State the blood parasite species.
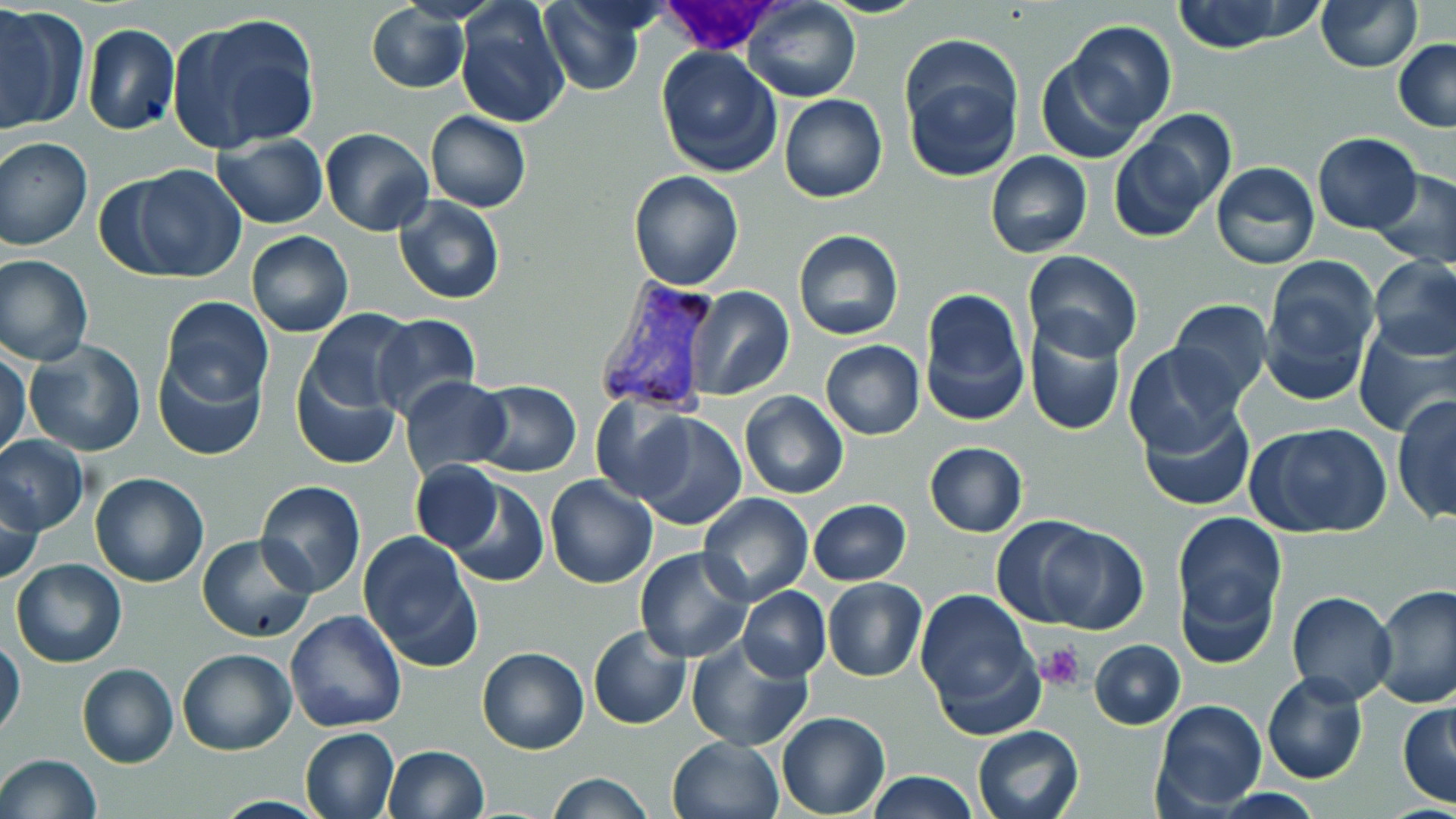

Plasmodium vivax.

Summary:
  - Coordinate format: approximate bounding boxes as [x1, y1, x2, y2] in pixels
  - Platelet locations: [1036, 643, 1085, 691]
  - Plasmodium vivax-infected red blood cell locations: [593, 275, 721, 415]
  - White blood cell locations: [650, 0, 794, 57]
  - Uninfected red blood cell locations: [538, 0, 651, 96], [745, 0, 859, 102], [1316, 0, 1421, 72], [455, 1, 572, 129], [1170, 1, 1319, 54], [0, 4, 87, 133], [367, 4, 471, 93], [169, 13, 322, 153], [1065, 21, 1178, 132], [82, 24, 179, 135], [1393, 39, 1456, 131], [899, 44, 1022, 182], [655, 45, 783, 177], [1034, 54, 1146, 165], [779, 94, 887, 202], [425, 109, 531, 212], [321, 127, 433, 237], [1109, 127, 1224, 240], [213, 133, 329, 229], [1312, 133, 1423, 234], [0, 136, 93, 251], [141, 148, 321, 254], [985, 150, 1092, 258], [1210, 162, 1320, 269], [123, 164, 247, 282], [1372, 169, 1456, 266], [627, 170, 745, 292], [393, 196, 506, 306], [793, 230, 903, 340], [246, 231, 352, 337], [1023, 250, 1143, 360], [1, 254, 94, 367], [1368, 255, 1456, 361], [1259, 257, 1379, 404], [684, 286, 794, 399], [917, 288, 1029, 427], [159, 296, 274, 404], [1167, 299, 1273, 403], [302, 308, 420, 418], [370, 312, 483, 420], [1023, 320, 1128, 438], [1354, 325, 1454, 436], [1025, 328, 1242, 441], [25, 339, 145, 457], [820, 339, 924, 440], [1124, 343, 1246, 456], [0, 346, 29, 461], [154, 352, 266, 461], [290, 358, 403, 470], [401, 375, 511, 481], [471, 379, 582, 476], [740, 391, 848, 499], [1392, 393, 1456, 525], [591, 398, 702, 502], [1139, 403, 1255, 512], [629, 412, 747, 532], [1245, 421, 1394, 539], [0, 435, 87, 535], [923, 441, 1028, 536], [411, 461, 503, 553], [434, 471, 552, 588], [89, 472, 211, 587], [545, 476, 659, 589], [1, 480, 45, 586], [255, 480, 366, 597], [697, 492, 813, 607], [808, 500, 911, 585], [1173, 511, 1286, 642], [991, 515, 1104, 626], [1034, 526, 1150, 634], [358, 531, 484, 674], [195, 532, 317, 644], [633, 548, 754, 663], [10, 558, 127, 668], [1177, 568, 1281, 671], [822, 578, 927, 682], [1371, 581, 1456, 707], [737, 586, 830, 681], [915, 587, 1039, 727], [1285, 591, 1398, 705], [284, 610, 409, 733], [588, 625, 690, 731], [686, 635, 814, 752], [0, 636, 26, 739], [1090, 639, 1186, 729], [476, 646, 589, 755], [177, 648, 296, 755], [77, 663, 178, 767], [1261, 671, 1369, 785], [1153, 700, 1267, 814], [1397, 700, 1456, 808], [776, 711, 889, 817], [972, 723, 1085, 819], [300, 728, 400, 818], [667, 735, 784, 819], [382, 745, 489, 819], [0, 753, 101, 819], [866, 771, 980, 818], [546, 773, 653, 818]
  - Field of view: one of a larger specimen
  - Preparation: thin blood film
  - Image size: 1456×819 pixels
  - Stain: May-Grünwald-Giemsa
  - Magnification: 1000x
  - Modality: optical microscopy